Assess this cell for malaria.
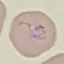
Parasitized.

Summary:
  - Image type: automatically extracted cell patch, resized to 64 × 64 pixels
  - Preparation: thin blood film
  - Capture: smartphone camera at the microscope eyepiece
  - Stain: Giemsa